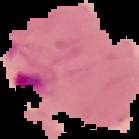
From a thin blood smear. Result: Plasmodium parasites detected. Cell region segmented out of the field of view; the surrounding area is masked to black. Image is 139×139 pixels.